Classify this cell by malaria status.
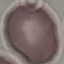

Uninfected.

Summary:
  - Capture: smartphone through the microscope eyepiece
  - Preparation: thin blood film
  - Stain: Giemsa
  - Image type: cell patch, automatically extracted from a larger field of view and resized to 64 × 64 pixels